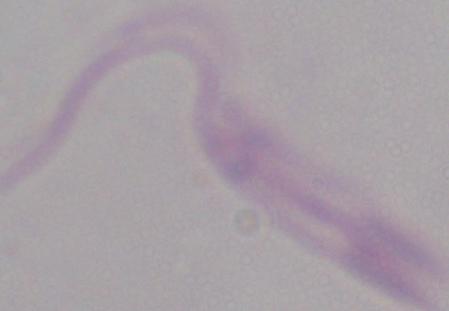
identification = Leishmania
modality = photomicrograph
magnification = 1000x